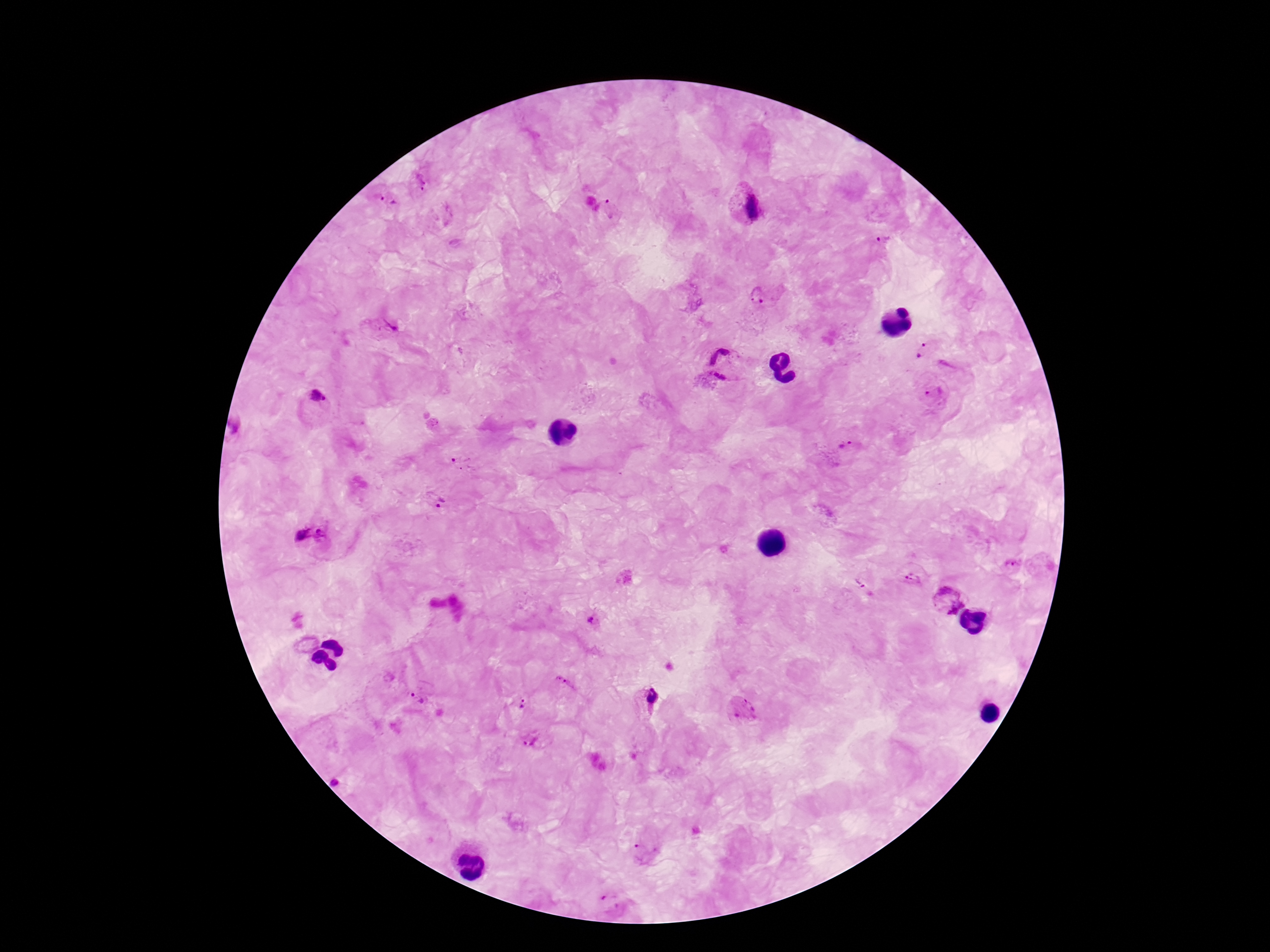
plasmodium_parasite_locations: 'approximate centers as {x, y} in pixels: {419, 183}, {387, 203}, {743, 205}, {612, 208}, {884, 239}, {759, 296}, {381, 329}, {923, 348}, {723, 364}, {935, 394}, {318, 401}, {846, 446}, {464, 462}, {438, 500}, {312, 538}, {1012, 566}, {912, 578}, {858, 583}, {945, 602}, {591, 621}, {564, 685}, {418, 699}, {647, 700}, {522, 704}, {742, 711}, {531, 740}, {339, 781}, {646, 852}, {610, 902}'
field_of_view: one from this slide
capture: smartphone camera through the microscope eyepiece
preparation: thick peripheral-blood smear
magnification: 100x
patient_malaria_status: positive
stain: Giemsa
image_size: 1270×952 pixels